Outline each blood parasite and name the species.
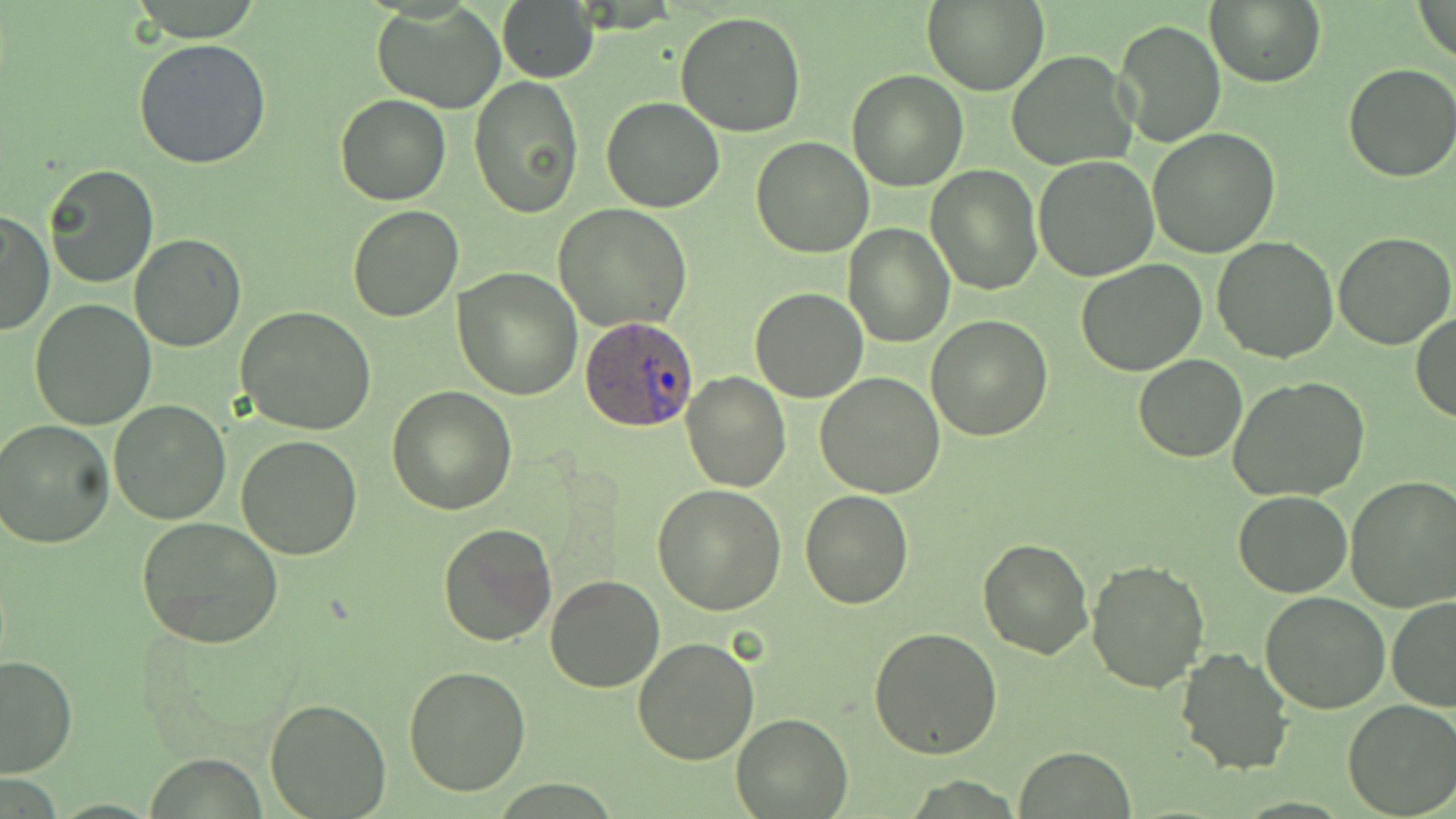

Approximate bounding boxes as [x1, y1, x2, y2] in pixels.
Plasmodium ovale-infected red blood cells: [578, 315, 699, 433].
No Plasmodium falciparum, Plasmodium malariae, Plasmodium vivax, Babesia divergens, or Trypanosoma brucei observed.

slide-level diagnosis = Plasmodium ovale
stain = May-Grünwald-Giemsa
modality = optical microscopy
preparation = thin blood smear
uninfected red blood cell locations = approximate bounding boxes as [x1, y1, x2, y2] in pixels: [497, 0, 599, 84], [922, 0, 1048, 95], [1206, 0, 1325, 89], [1414, 0, 1456, 67], [373, 4, 506, 114], [676, 10, 806, 137], [1115, 19, 1226, 148], [136, 37, 272, 170], [1006, 51, 1136, 170], [1342, 63, 1456, 183], [845, 70, 967, 191], [470, 75, 584, 218], [334, 93, 451, 206], [600, 96, 726, 213], [1147, 128, 1281, 258], [751, 137, 873, 258], [1033, 156, 1160, 282], [43, 164, 159, 288], [925, 165, 1042, 295], [555, 203, 692, 332], [346, 206, 463, 323], [0, 210, 53, 336], [842, 224, 955, 348], [1334, 231, 1454, 348], [129, 233, 246, 351], [1212, 236, 1337, 362], [1077, 259, 1206, 375], [453, 266, 583, 399], [749, 287, 866, 402], [30, 298, 158, 430], [235, 307, 376, 436], [1412, 311, 1456, 422], [926, 316, 1052, 441], [1132, 355, 1247, 462], [681, 373, 790, 492], [815, 373, 945, 497], [1228, 375, 1372, 501], [387, 385, 515, 514], [109, 399, 231, 523], [0, 420, 115, 549], [237, 434, 362, 558], [1345, 476, 1456, 613], [652, 483, 786, 616], [800, 490, 915, 609], [1233, 491, 1353, 597], [137, 518, 284, 649], [437, 521, 557, 647], [976, 537, 1093, 658], [1086, 560, 1209, 694], [544, 573, 667, 693], [1260, 592, 1389, 713], [1387, 595, 1456, 711], [869, 628, 1005, 757], [632, 636, 759, 766], [1174, 647, 1292, 774], [1, 654, 77, 777], [403, 666, 531, 796], [264, 698, 391, 818], [1341, 699, 1456, 819], [731, 711, 852, 817], [1014, 747, 1136, 818]
image size = 1456×819 pixels
magnification = 1000x
field of view = single